State which parasite is depicted.
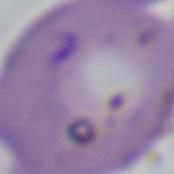
Babesia.

Photomicrograph. 1000x magnification.